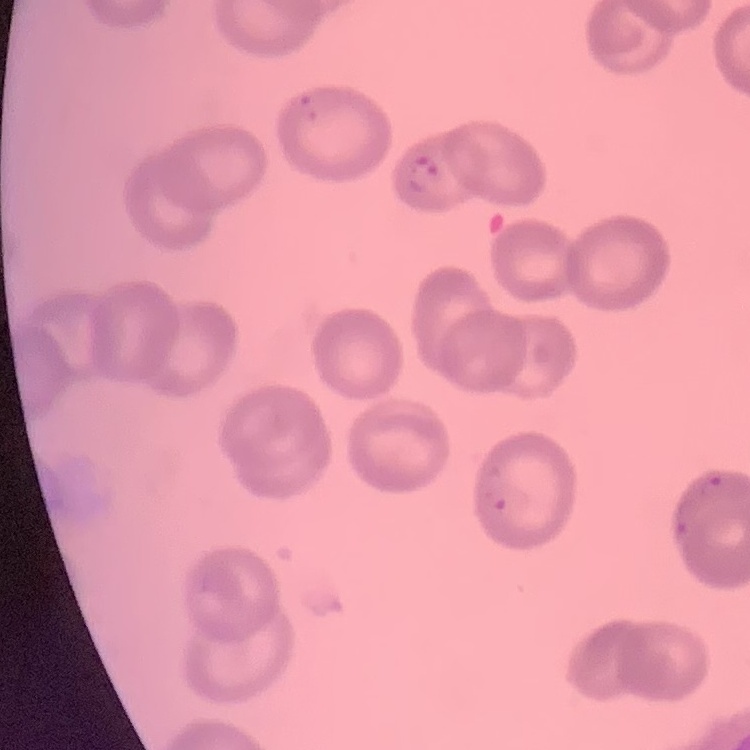

red blood cell morphology = no rouleaux formation
stain = Field's or Giemsa
preparation = thin blood smear
image type = one tile cut from a larger photomicrograph